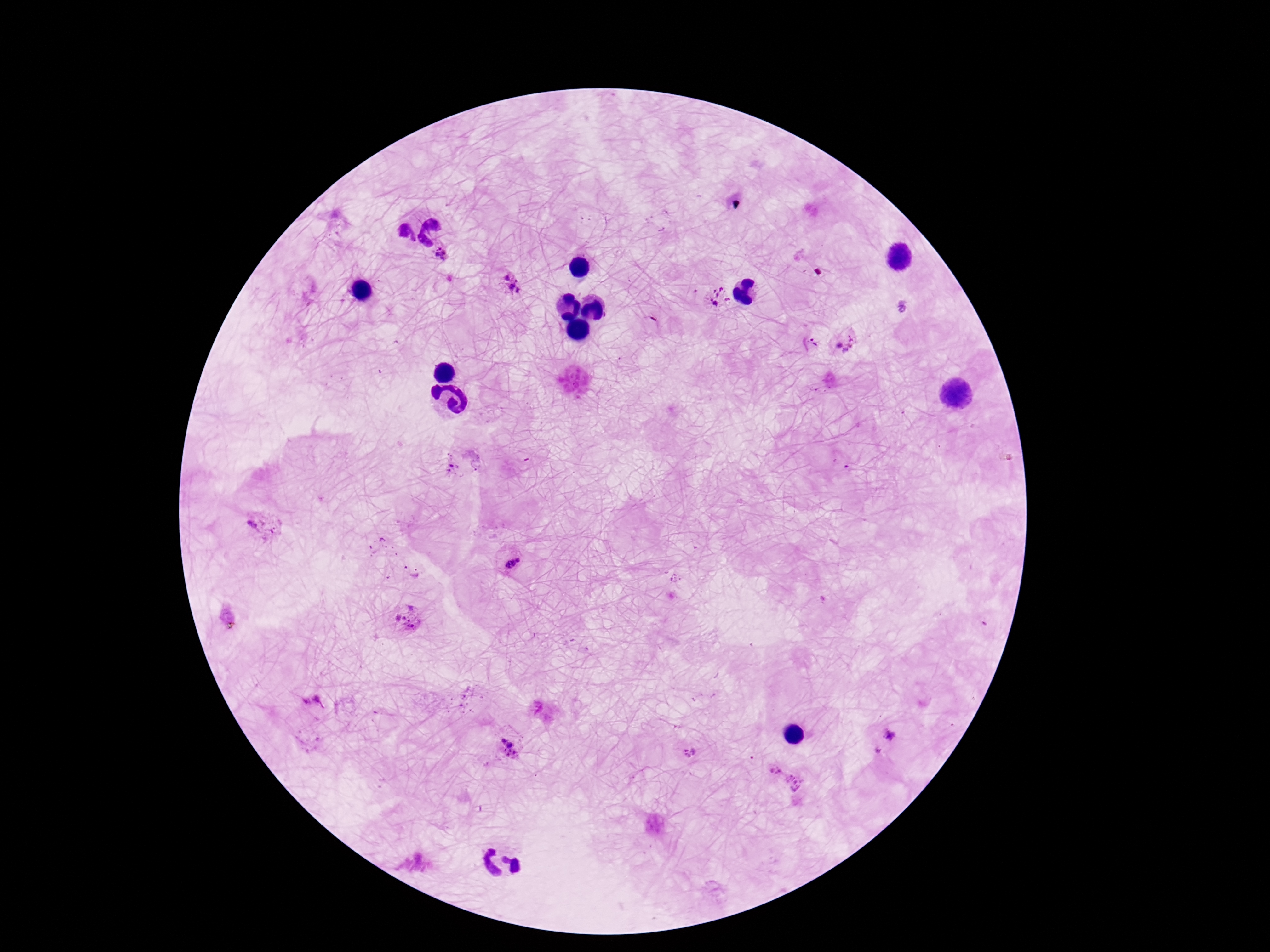 Approximate centers as {x, y} in pixels. Plasmodium parasite locations: {442, 254}, {509, 280}, {719, 298}, {847, 342}, {812, 343}, {263, 527}, {511, 562}, {408, 618}, {228, 619}, {313, 701}, {892, 737}, {508, 748}, {690, 753}, {784, 776}. Giemsa-stained preparation. 100x magnification. Patient malaria status: positive. Single field of view. Image is 1270×952 pixels. Smartphone photograph taken through the microscope eyepiece. Thick blood smear.